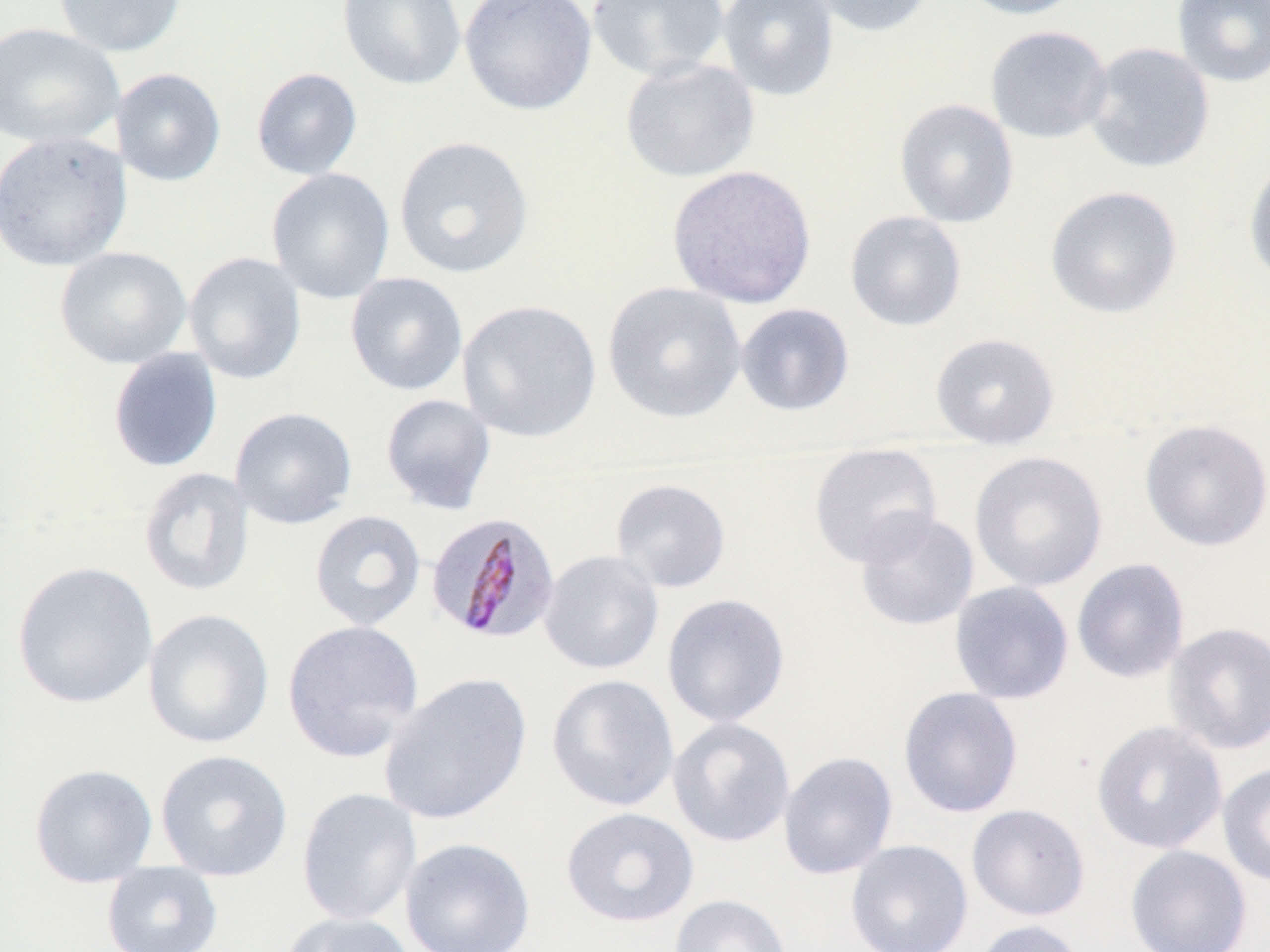

Summary:
  - Coordinate format: approximate bounding boxes as named x1/y1/x2/y2 corners in pixels
  - Uninfected red blood cell locations: (x1=53, y1=0, x2=187, y2=57), (x1=336, y1=0, x2=467, y2=92), (x1=460, y1=0, x2=597, y2=116), (x1=587, y1=0, x2=731, y2=82), (x1=717, y1=0, x2=839, y2=102), (x1=806, y1=0, x2=936, y2=37), (x1=955, y1=0, x2=1087, y2=20), (x1=1172, y1=0, x2=1270, y2=88), (x1=0, y1=22, x2=125, y2=150), (x1=985, y1=24, x2=1113, y2=144), (x1=1084, y1=42, x2=1215, y2=174), (x1=620, y1=57, x2=760, y2=182), (x1=111, y1=68, x2=227, y2=186), (x1=251, y1=68, x2=363, y2=180), (x1=894, y1=98, x2=1019, y2=228), (x1=0, y1=130, x2=133, y2=272), (x1=393, y1=135, x2=534, y2=279), (x1=1244, y1=155, x2=1270, y2=287), (x1=667, y1=165, x2=817, y2=309), (x1=266, y1=167, x2=395, y2=304), (x1=1045, y1=185, x2=1182, y2=319), (x1=845, y1=210, x2=967, y2=332), (x1=55, y1=246, x2=192, y2=369), (x1=183, y1=251, x2=306, y2=385), (x1=345, y1=272, x2=468, y2=395), (x1=602, y1=281, x2=747, y2=423), (x1=457, y1=298, x2=602, y2=443), (x1=735, y1=303, x2=855, y2=416), (x1=930, y1=332, x2=1060, y2=447), (x1=108, y1=347, x2=223, y2=473), (x1=380, y1=393, x2=497, y2=514), (x1=230, y1=407, x2=357, y2=529), (x1=1139, y1=419, x2=1270, y2=551), (x1=808, y1=447, x2=942, y2=568), (x1=969, y1=450, x2=1108, y2=592), (x1=138, y1=467, x2=256, y2=597), (x1=610, y1=478, x2=732, y2=593), (x1=853, y1=508, x2=979, y2=631), (x1=309, y1=509, x2=427, y2=631), (x1=538, y1=550, x2=665, y2=674), (x1=1071, y1=558, x2=1190, y2=683), (x1=11, y1=560, x2=159, y2=710), (x1=949, y1=581, x2=1074, y2=704), (x1=662, y1=593, x2=790, y2=728), (x1=142, y1=608, x2=275, y2=749), (x1=282, y1=620, x2=425, y2=763), (x1=1163, y1=621, x2=1270, y2=754), (x1=378, y1=673, x2=532, y2=825), (x1=546, y1=673, x2=679, y2=812), (x1=898, y1=686, x2=1023, y2=819), (x1=667, y1=717, x2=795, y2=848), (x1=1091, y1=720, x2=1228, y2=854), (x1=155, y1=749, x2=293, y2=881), (x1=778, y1=751, x2=898, y2=879), (x1=1217, y1=762, x2=1270, y2=888), (x1=28, y1=763, x2=158, y2=888), (x1=296, y1=787, x2=422, y2=926), (x1=966, y1=804, x2=1091, y2=921), (x1=561, y1=807, x2=699, y2=928), (x1=399, y1=837, x2=536, y2=951), (x1=845, y1=839, x2=973, y2=952), (x1=1124, y1=844, x2=1252, y2=952), (x1=101, y1=860, x2=224, y2=952), (x1=668, y1=893, x2=792, y2=952), (x1=280, y1=911, x2=419, y2=952), (x1=971, y1=920, x2=1088, y2=952)
  - Plasmodium malariae-infected red blood cell locations: (x1=427, y1=510, x2=563, y2=645)
  - Slide-level diagnosis: Plasmodium malariae
  - Image size: 1270×952 pixels
  - Magnification: 1000x
  - Stain: May-Grünwald-Giemsa
  - Field of view: one of a larger specimen
  - Modality: optical microscopy
  - Preparation: thin blood smear